Assess the morphology of the erythrocytes.
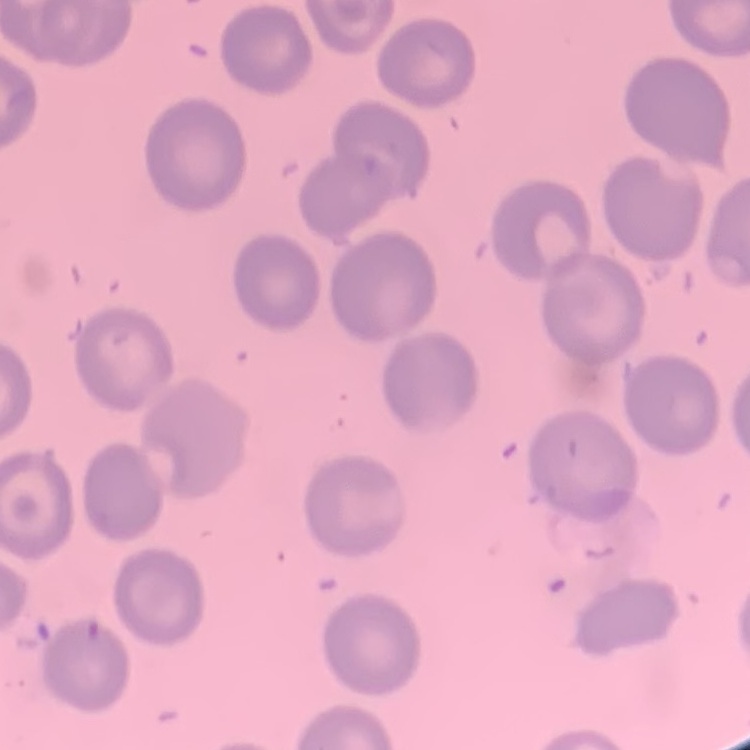

No rouleaux formation.

Square crop of a larger photomicrograph. Stained with either Field's or Giemsa. Thin peripheral smear.